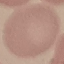

Summary:
  - Result: no malaria parasites detected
  - Preparation: thin blood film
  - Stain: Giemsa
  - Image type: cell patch, automatically extracted from a larger field of view and resized to 64 × 64 pixels
  - Capture: smartphone camera at the microscope eyepiece